Identify the parasite.
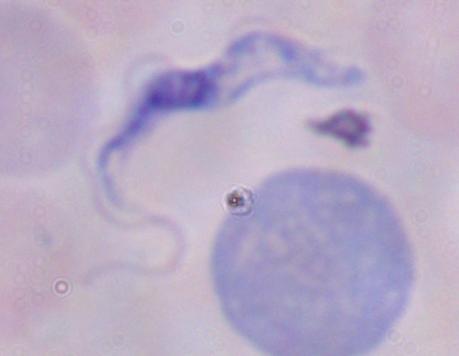
This is a trypanosome.

Captured at 1000x magnification. Photomicrograph.